Identify the parasite.
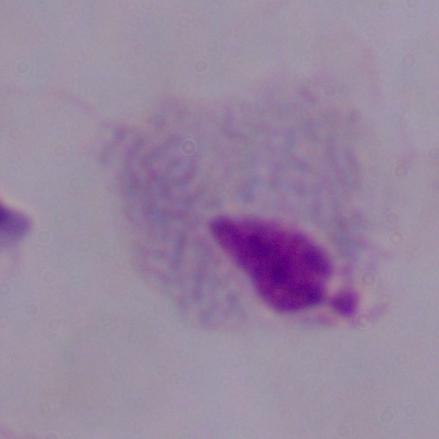

This is a trichomonad.

magnification: 1000x
modality: micrograph